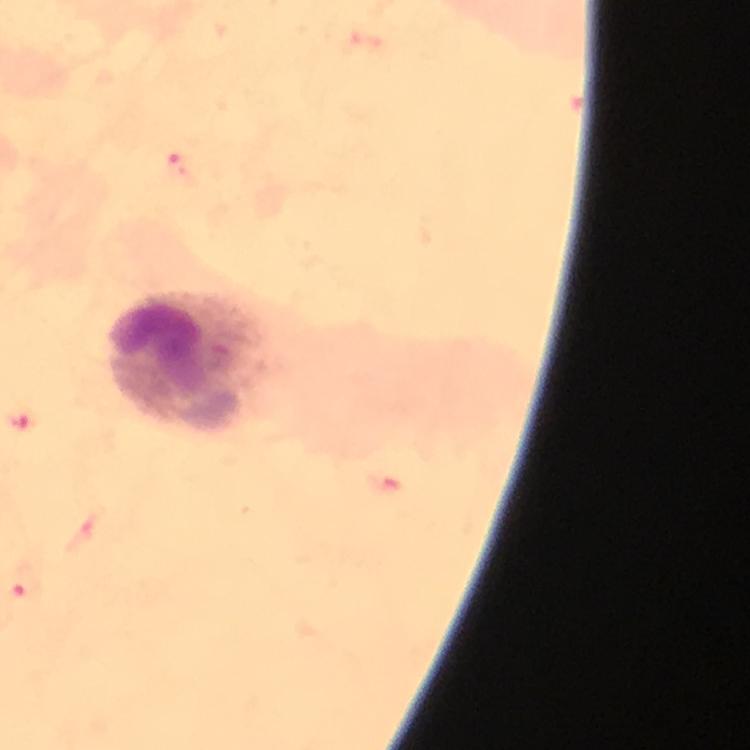
Approximate centers as [x, y] in pixels. Malaria parasite locations: [182, 169], [24, 420], [26, 582]. Leukocyte locations: [190, 365]. At 100x magnification. Thick blood film. From a diagnostic examination for malaria. Immersion oil applied. Image is 750×750 pixels. Photographed through the microscope with a smartphone camera. Giemsa-stained preparation. A crop from one field of view.